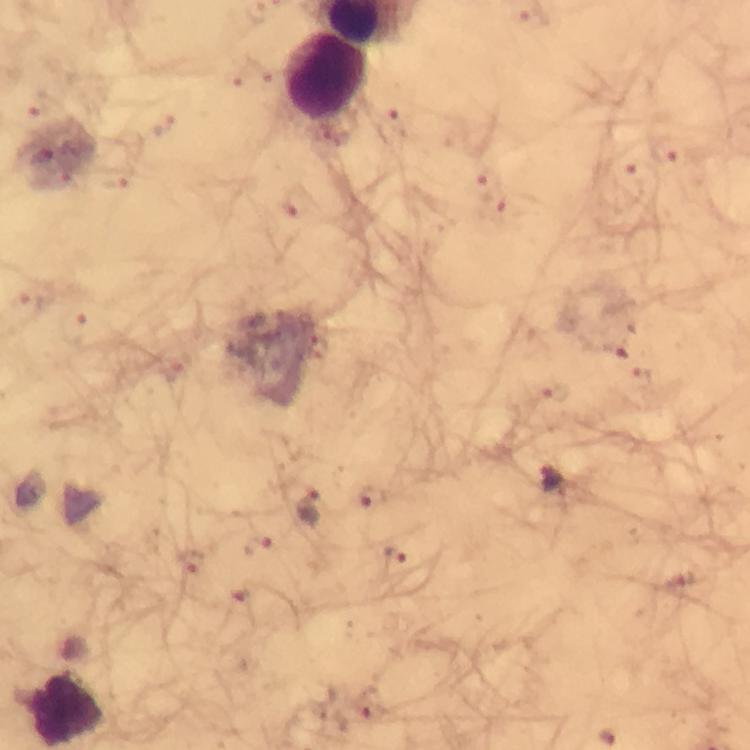 Approximate centers as [x, y] in pixels. Plasmodium parasite locations: [164, 125], [393, 125], [667, 152], [626, 171], [116, 183], [485, 185], [293, 201], [30, 303], [74, 329], [315, 344], [615, 347], [642, 379], [556, 395], [556, 480], [369, 497], [312, 505], [255, 545], [395, 555], [191, 562], [678, 586], [373, 706]. Leukocyte locations: [324, 78], [68, 709]. At 100x magnification. Photographed with a smartphone mounted on the microscope. Image is 750×750 pixels. Thick smear. From a malaria diagnostic workup. Giemsa stain. Immersion oil applied. A crop from one field of view.